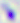
Toxoplasma gondii is seen. 400x magnification. Micrograph.